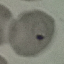
Summary:
  - Result: malaria parasites identified
  - Image type: cell patch, automatically extracted from a larger field of view and resized to 64 × 64 pixels
  - Preparation: thin blood film
  - Capture: smartphone through the microscope eyepiece
  - Stain: Giemsa